State which parasite is depicted.
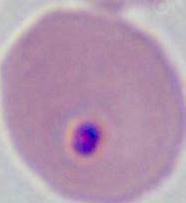
This is Plasmodium.

{
  "modality": "photomicrograph",
  "magnification": "400x or 1000x"
}